State the preparation type.
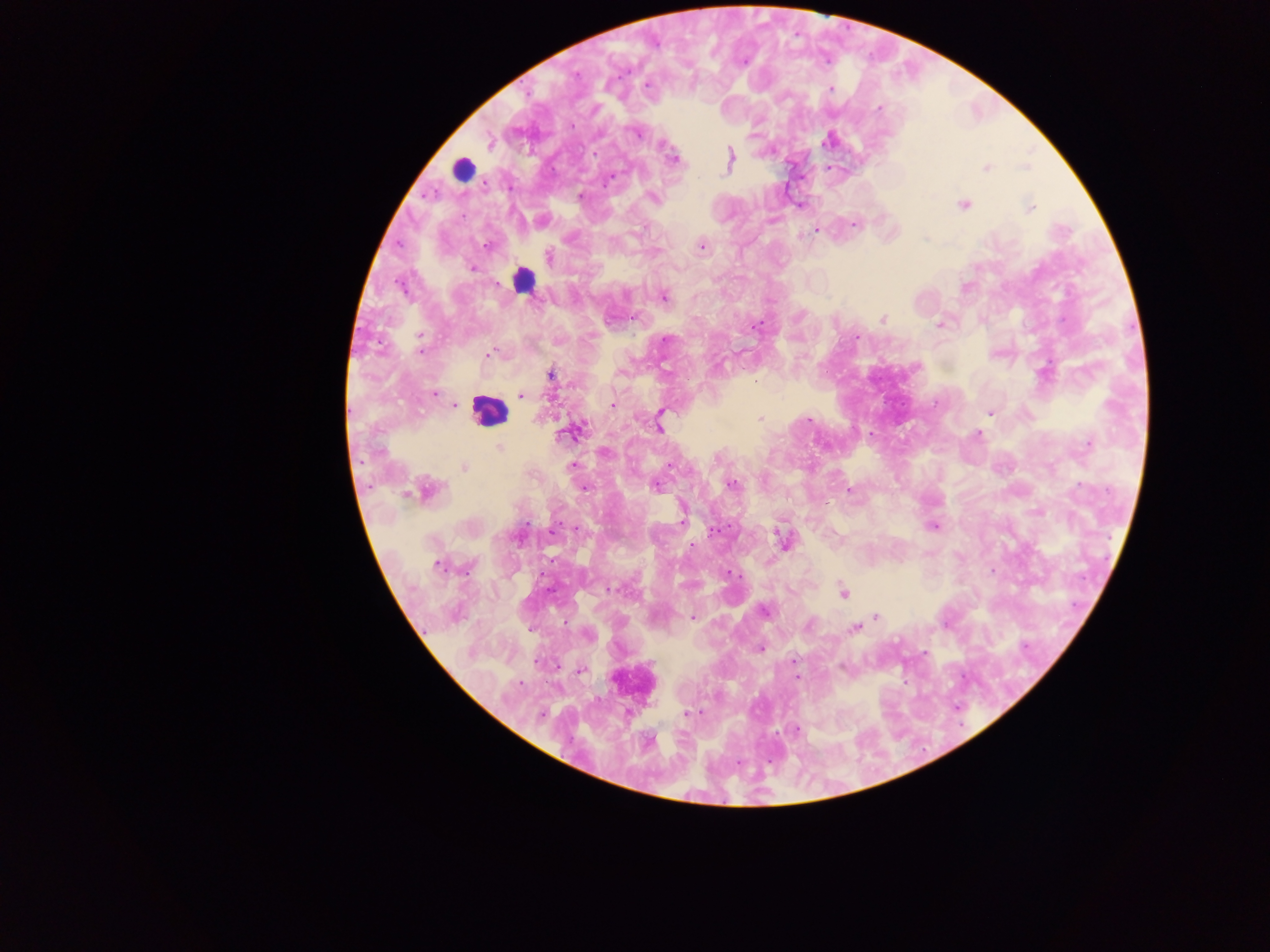
Thick blood film.

Approximate centers as x y in pixels. Plasmodium parasite locations: 743 63; 647 86; 831 89; 879 109; 635 133; 828 140; 489 142; 662 145; 673 159; 730 161; 986 167; 1024 168; 428 195; 580 196; 654 197; 799 205; 963 205; 1030 208; 854 224; 815 231; 487 245; 701 246; 549 256; 472 269; 401 287; 664 297; 882 318; 939 324; 755 326; 420 336; 856 339; 665 340; 421 350; 490 354; 549 374; 435 394; 520 395; 455 405; 612 405; 990 412; 660 414; 759 418; 809 420; 659 425; 567 434; 977 435; 1087 445; 499 448; 604 453; 572 466; 464 467; 656 485; 732 485; 584 488; 427 490; 849 491; 682 521; 934 526; 714 531; 782 540; 694 544; 437 565; 729 572; 610 588; 843 592; 765 610; 877 617; 692 618; 809 625; 854 629; 760 650; 794 661; 581 671; 520 683; 687 713; 797 729. Leukocyte locations: 462 170; 522 280; 488 411. Collected in Ghana. Photographed through a microscope with a mobile-phone camera. Single field of view. Image is 1270×952 pixels.